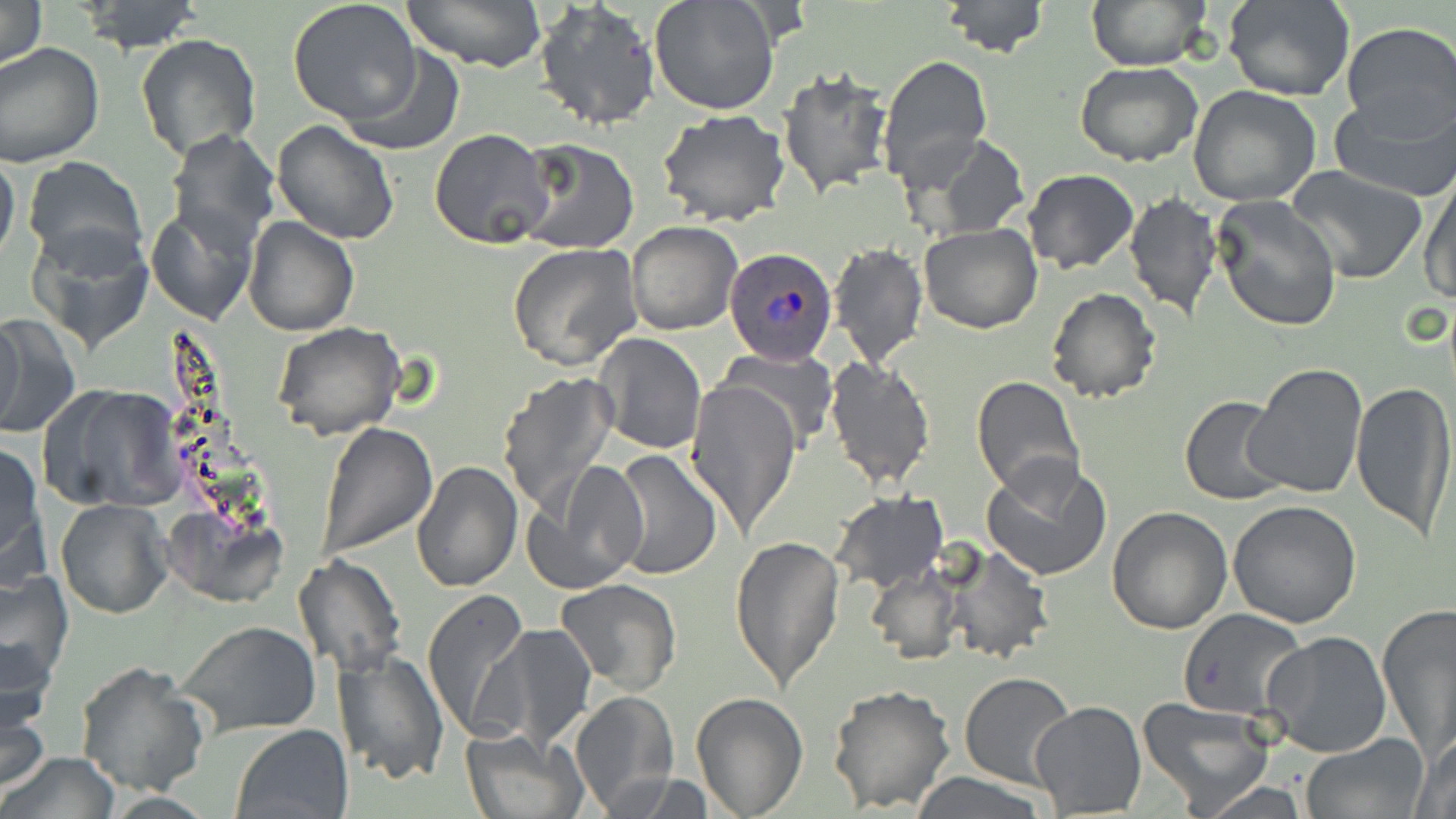
{
  "slide_level_diagnosis": "Plasmodium ovale",
  "preparation": "thin blood film",
  "uninfected_red_blood_cell_locations": "approximate bounding boxes as (x1, y1, x2, y2) in pixels: (0, 0, 48, 73), (287, 0, 423, 125), (400, 0, 549, 71), (649, 0, 782, 117), (938, 0, 1051, 57), (1087, 0, 1210, 70), (79, 1, 203, 54), (1224, 1, 1353, 102), (534, 2, 660, 130), (1340, 22, 1455, 133), (135, 32, 262, 162), (0, 43, 104, 167), (341, 46, 464, 157), (878, 55, 992, 185), (1075, 61, 1203, 165), (777, 67, 894, 199), (1188, 85, 1322, 207), (1329, 87, 1456, 201), (658, 108, 790, 226), (271, 120, 401, 244), (166, 128, 280, 252), (430, 128, 555, 249), (914, 133, 1031, 244), (513, 139, 639, 255), (0, 151, 20, 270), (23, 157, 147, 272), (1285, 165, 1429, 285), (1024, 168, 1138, 273), (1418, 169, 1456, 306), (1124, 193, 1222, 320), (1214, 196, 1341, 332), (148, 205, 259, 323), (242, 217, 358, 336), (626, 220, 744, 335), (30, 223, 153, 357), (917, 224, 1042, 333), (830, 241, 929, 368), (506, 243, 643, 373), (1044, 287, 1162, 404), (1, 313, 28, 437), (0, 318, 81, 438), (272, 322, 405, 441), (592, 333, 708, 456), (722, 345, 836, 446), (824, 356, 936, 490), (1241, 361, 1367, 500), (495, 370, 618, 513), (971, 375, 1084, 497), (686, 376, 801, 537), (1351, 379, 1455, 539), (43, 384, 183, 510), (1178, 395, 1289, 505), (317, 422, 438, 558), (0, 442, 47, 585), (610, 449, 722, 579), (980, 455, 1112, 584), (527, 460, 647, 593), (411, 461, 523, 593), (831, 491, 947, 593), (55, 498, 173, 619), (1228, 499, 1362, 628), (1106, 505, 1233, 633), (729, 534, 845, 692), (938, 543, 1054, 665), (292, 555, 406, 677), (864, 565, 963, 666), (1, 569, 71, 689), (554, 579, 682, 696), (422, 588, 531, 741), (1377, 604, 1456, 753), (1178, 609, 1310, 718), (177, 620, 322, 738), (479, 624, 598, 751), (1261, 631, 1392, 758), (0, 634, 57, 736), (332, 650, 449, 787), (75, 660, 212, 797), (958, 672, 1076, 789), (828, 683, 957, 814), (0, 687, 51, 794), (568, 692, 680, 813), (690, 692, 809, 819), (1136, 696, 1274, 813), (1028, 702, 1146, 817), (230, 724, 353, 819), (460, 727, 585, 819), (1299, 734, 1430, 818), (1410, 734, 1456, 819), (4, 750, 120, 819), (613, 772, 722, 817), (907, 772, 1052, 818), (1187, 780, 1315, 818), (97, 791, 220, 819)",
  "stain": "May-Grünwald-Giemsa",
  "field_of_view": "single",
  "image_size": "1456×819 pixels",
  "plasmodium_ovale_infected_red_blood_cell_locations": "approximate bounding boxes as (x1, y1, x2, y2) in pixels: (724, 247, 838, 367)",
  "magnification": "1000x",
  "modality": "optical microscopy"
}